Mark where platelets are.
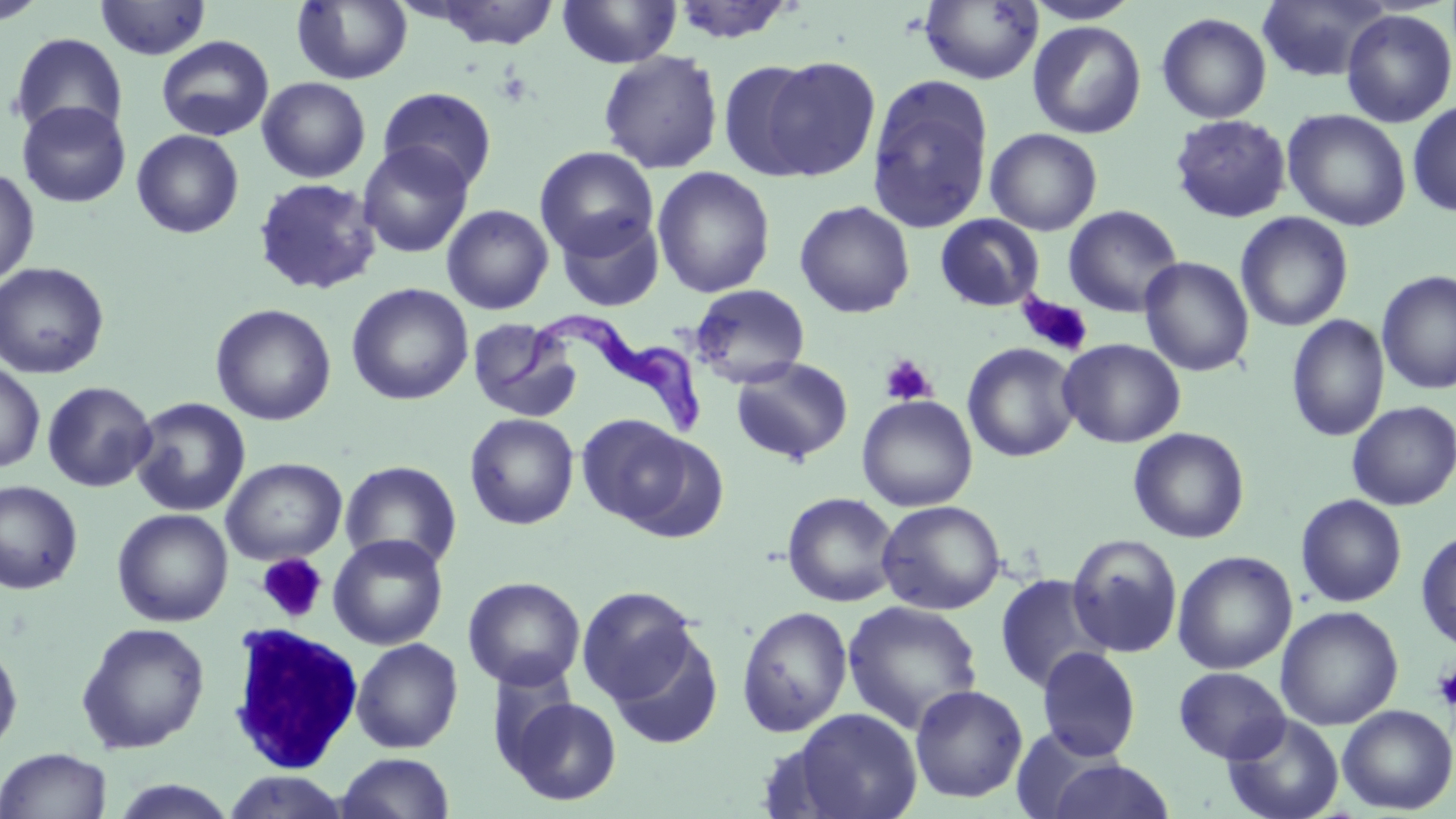
Approximate bounding boxes as named x1/y1/x2/y2 corners in pixels.
Platelets: (x1=1018, y1=294, x2=1093, y2=358), (x1=879, y1=355, x2=937, y2=406), (x1=257, y1=552, x2=328, y2=624), (x1=1432, y1=664, x2=1456, y2=711).

Summary:
  - White blood cell locations: (x1=227, y1=623, x2=365, y2=774)
  - Trypanosoma brucei locations: (x1=497, y1=312, x2=707, y2=435)
  - Uninfected red blood cell locations: (x1=1, y1=0, x2=49, y2=25), (x1=292, y1=0, x2=412, y2=85), (x1=557, y1=0, x2=681, y2=68), (x1=1023, y1=0, x2=1141, y2=25), (x1=1256, y1=0, x2=1390, y2=82), (x1=94, y1=1, x2=211, y2=60), (x1=425, y1=1, x2=562, y2=50), (x1=669, y1=1, x2=799, y2=44), (x1=918, y1=1, x2=1043, y2=85), (x1=1340, y1=8, x2=1456, y2=128), (x1=1156, y1=12, x2=1272, y2=124), (x1=1027, y1=21, x2=1146, y2=139), (x1=9, y1=32, x2=128, y2=141), (x1=156, y1=35, x2=274, y2=141), (x1=598, y1=51, x2=724, y2=174), (x1=759, y1=55, x2=881, y2=178), (x1=719, y1=59, x2=823, y2=181), (x1=867, y1=76, x2=994, y2=233), (x1=256, y1=77, x2=371, y2=183), (x1=378, y1=86, x2=498, y2=193), (x1=16, y1=100, x2=131, y2=209), (x1=1407, y1=101, x2=1456, y2=217), (x1=1282, y1=108, x2=1412, y2=232), (x1=1169, y1=114, x2=1292, y2=223), (x1=985, y1=128, x2=1103, y2=236), (x1=131, y1=129, x2=244, y2=239), (x1=357, y1=141, x2=474, y2=258), (x1=534, y1=146, x2=658, y2=259), (x1=652, y1=167, x2=775, y2=298), (x1=0, y1=168, x2=40, y2=287), (x1=252, y1=177, x2=382, y2=296), (x1=794, y1=200, x2=915, y2=319), (x1=441, y1=204, x2=554, y2=314), (x1=1063, y1=205, x2=1184, y2=318), (x1=556, y1=211, x2=665, y2=313), (x1=1235, y1=211, x2=1354, y2=332), (x1=934, y1=214, x2=1046, y2=312), (x1=1139, y1=256, x2=1254, y2=376), (x1=0, y1=261, x2=110, y2=380), (x1=1376, y1=270, x2=1456, y2=395), (x1=346, y1=283, x2=474, y2=406), (x1=690, y1=283, x2=810, y2=387), (x1=210, y1=303, x2=336, y2=426), (x1=1286, y1=314, x2=1390, y2=442), (x1=467, y1=317, x2=582, y2=422), (x1=1058, y1=338, x2=1186, y2=448), (x1=962, y1=342, x2=1082, y2=462), (x1=731, y1=357, x2=853, y2=464), (x1=0, y1=362, x2=46, y2=474), (x1=41, y1=381, x2=157, y2=492), (x1=856, y1=395, x2=978, y2=512), (x1=129, y1=397, x2=251, y2=517), (x1=1346, y1=401, x2=1456, y2=511), (x1=464, y1=413, x2=579, y2=530), (x1=575, y1=414, x2=697, y2=529), (x1=1128, y1=427, x2=1250, y2=544), (x1=221, y1=457, x2=347, y2=566), (x1=339, y1=460, x2=462, y2=572), (x1=0, y1=480, x2=84, y2=595), (x1=782, y1=492, x2=901, y2=607), (x1=1295, y1=494, x2=1407, y2=608), (x1=876, y1=499, x2=1006, y2=615), (x1=112, y1=508, x2=234, y2=627), (x1=1416, y1=529, x2=1456, y2=652), (x1=328, y1=533, x2=448, y2=650), (x1=1067, y1=534, x2=1183, y2=659), (x1=1172, y1=550, x2=1297, y2=675), (x1=994, y1=573, x2=1112, y2=694), (x1=463, y1=577, x2=586, y2=691), (x1=576, y1=585, x2=698, y2=704), (x1=841, y1=600, x2=984, y2=734), (x1=1275, y1=605, x2=1404, y2=731), (x1=737, y1=606, x2=852, y2=736), (x1=75, y1=622, x2=210, y2=753), (x1=607, y1=630, x2=724, y2=750), (x1=350, y1=638, x2=464, y2=753), (x1=0, y1=642, x2=23, y2=760), (x1=1037, y1=647, x2=1141, y2=761), (x1=1173, y1=666, x2=1291, y2=763), (x1=909, y1=684, x2=1029, y2=804), (x1=503, y1=695, x2=623, y2=806), (x1=1337, y1=704, x2=1456, y2=814), (x1=788, y1=708, x2=921, y2=819), (x1=1222, y1=714, x2=1344, y2=819), (x1=0, y1=747, x2=112, y2=819), (x1=337, y1=752, x2=455, y2=819), (x1=1043, y1=759, x2=1176, y2=818), (x1=222, y1=771, x2=350, y2=818), (x1=108, y1=779, x2=239, y2=818)
  - Slide-level diagnosis: Trypanosoma brucei
  - Field of view: one of a larger specimen
  - Preparation: thin blood film
  - Stain: May-Grünwald-Giemsa
  - Modality: optical microscopy
  - Magnification: 1000x
  - Image size: 1456×819 pixels